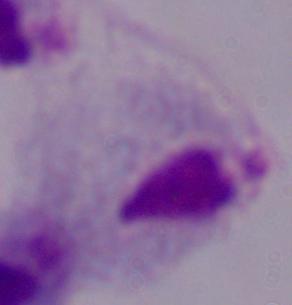
{
  "magnification": "1000x",
  "modality": "micrograph",
  "identification": "trichomonad"
}